Report the malaria status of this cell.
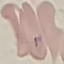
Uninfected.

Thin blood smear. Cell patch, automatically extracted from a larger field of view and resized to 64 × 64 pixels. Photographed with a smartphone camera at the microscope eyepiece. Giemsa stain.